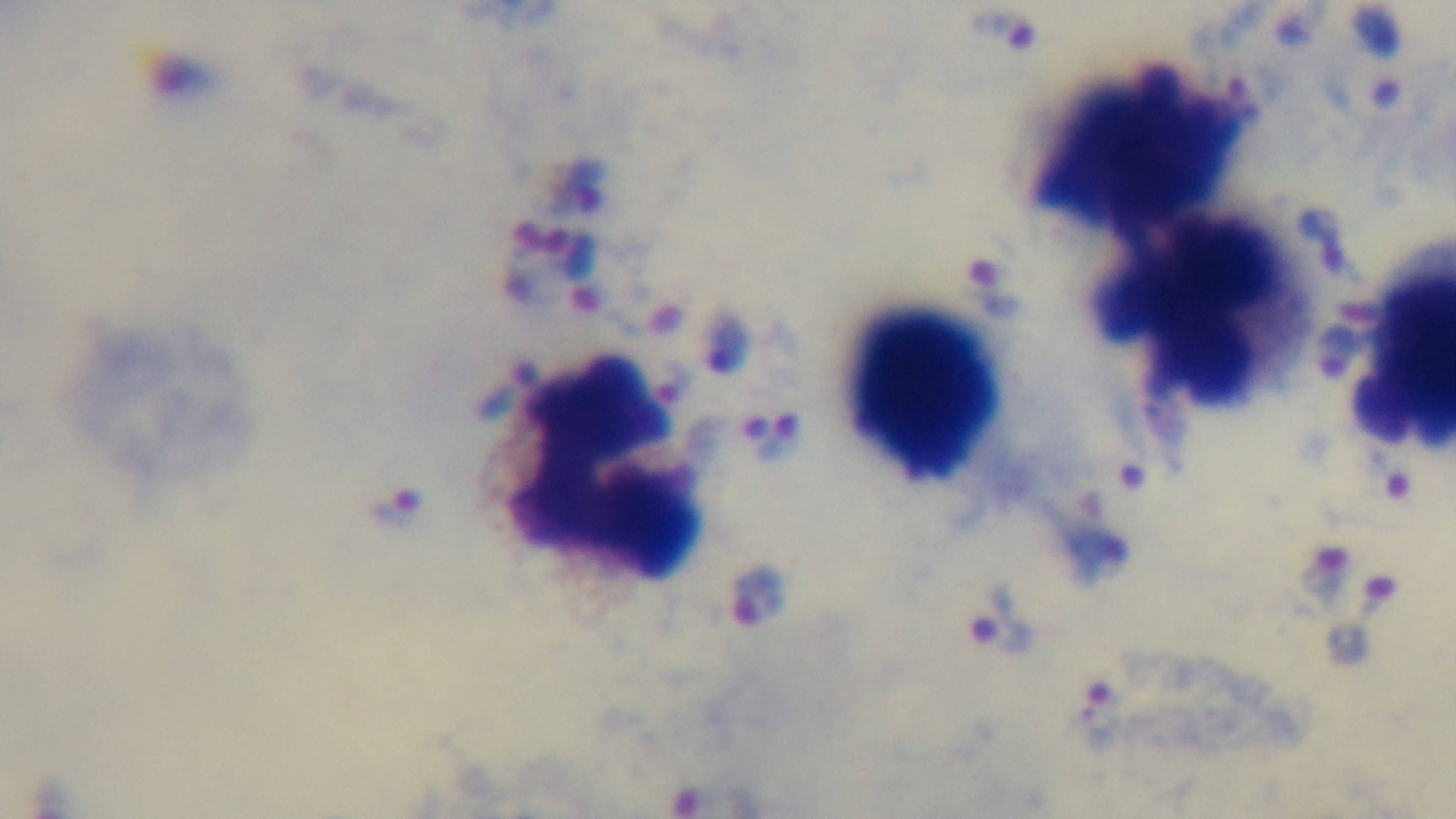

objective = 100x oil immersion
field of view = single
modality = light microscopy
stain = Giemsa
capture = mounted 4K digital camera
malaria status = positive
preparation = thick